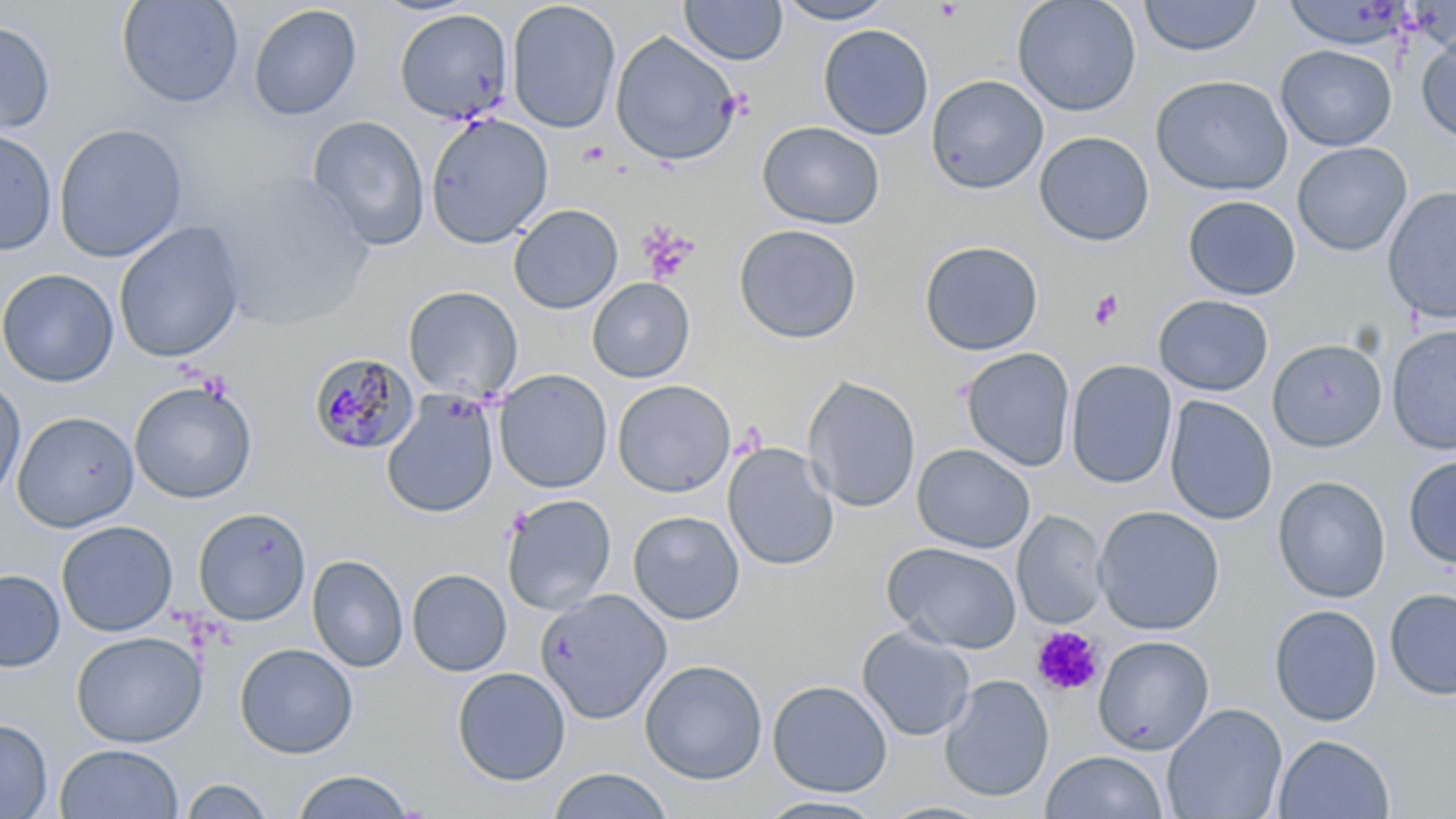
Summary:
  - Coordinate format: approximate bounding boxes as named x1/y1/x2/y2 corners in pixels
  - Platelet locations: (x1=637, y1=222, x2=699, y2=285), (x1=1088, y1=289, x2=1124, y2=330), (x1=1032, y1=626, x2=1105, y2=697)
  - Plasmodium malariae-infected red blood cell locations: (x1=308, y1=352, x2=419, y2=455)
  - Uninfected red blood cell locations: (x1=117, y1=0, x2=244, y2=108), (x1=679, y1=0, x2=788, y2=65), (x1=774, y1=0, x2=897, y2=25), (x1=1012, y1=0, x2=1142, y2=117), (x1=1138, y1=0, x2=1263, y2=57), (x1=506, y1=1, x2=621, y2=134), (x1=248, y1=4, x2=362, y2=121), (x1=394, y1=9, x2=514, y2=125), (x1=0, y1=20, x2=56, y2=135), (x1=818, y1=24, x2=934, y2=140), (x1=610, y1=30, x2=742, y2=166), (x1=1416, y1=32, x2=1456, y2=145), (x1=1275, y1=44, x2=1397, y2=151), (x1=926, y1=74, x2=1049, y2=194), (x1=1150, y1=74, x2=1293, y2=196), (x1=425, y1=113, x2=553, y2=249), (x1=307, y1=115, x2=430, y2=250), (x1=757, y1=121, x2=885, y2=229), (x1=53, y1=123, x2=189, y2=263), (x1=0, y1=128, x2=57, y2=255), (x1=1034, y1=131, x2=1154, y2=246), (x1=1292, y1=141, x2=1412, y2=256), (x1=206, y1=173, x2=378, y2=332), (x1=1382, y1=186, x2=1456, y2=325), (x1=1183, y1=195, x2=1301, y2=300), (x1=509, y1=204, x2=623, y2=314), (x1=112, y1=221, x2=247, y2=364), (x1=733, y1=223, x2=862, y2=344), (x1=919, y1=240, x2=1044, y2=356), (x1=0, y1=268, x2=119, y2=387), (x1=587, y1=277, x2=695, y2=383), (x1=403, y1=286, x2=523, y2=401), (x1=1153, y1=294, x2=1274, y2=396), (x1=1386, y1=323, x2=1456, y2=455), (x1=1267, y1=338, x2=1388, y2=452), (x1=961, y1=347, x2=1076, y2=471), (x1=1066, y1=360, x2=1177, y2=489), (x1=494, y1=369, x2=612, y2=493), (x1=0, y1=375, x2=26, y2=503), (x1=802, y1=375, x2=921, y2=513), (x1=129, y1=379, x2=257, y2=503), (x1=612, y1=379, x2=737, y2=498), (x1=381, y1=390, x2=500, y2=518), (x1=1164, y1=395, x2=1278, y2=525), (x1=12, y1=411, x2=140, y2=533), (x1=722, y1=442, x2=839, y2=571), (x1=912, y1=443, x2=1035, y2=554), (x1=1403, y1=455, x2=1456, y2=569), (x1=1273, y1=475, x2=1391, y2=603), (x1=501, y1=494, x2=617, y2=615), (x1=1092, y1=505, x2=1225, y2=635), (x1=193, y1=507, x2=311, y2=626), (x1=628, y1=510, x2=745, y2=625), (x1=1013, y1=510, x2=1108, y2=629), (x1=56, y1=520, x2=178, y2=637), (x1=882, y1=541, x2=1022, y2=653), (x1=307, y1=554, x2=409, y2=672), (x1=406, y1=568, x2=512, y2=676), (x1=0, y1=569, x2=65, y2=672), (x1=1385, y1=588, x2=1456, y2=700), (x1=536, y1=589, x2=672, y2=724), (x1=1269, y1=604, x2=1383, y2=726), (x1=857, y1=626, x2=975, y2=741), (x1=71, y1=631, x2=206, y2=747), (x1=1092, y1=635, x2=1214, y2=755), (x1=234, y1=643, x2=358, y2=759), (x1=639, y1=659, x2=768, y2=784), (x1=452, y1=666, x2=571, y2=786), (x1=940, y1=674, x2=1054, y2=802), (x1=767, y1=679, x2=892, y2=797), (x1=1161, y1=703, x2=1288, y2=819), (x1=0, y1=718, x2=53, y2=818), (x1=1273, y1=733, x2=1396, y2=819), (x1=54, y1=743, x2=184, y2=819), (x1=1041, y1=751, x2=1168, y2=819), (x1=548, y1=768, x2=673, y2=819), (x1=290, y1=769, x2=416, y2=818), (x1=177, y1=776, x2=277, y2=818), (x1=755, y1=795, x2=888, y2=818)
  - Slide-level diagnosis: Plasmodium malariae
  - Modality: optical microscopy
  - Image size: 1456×819 pixels
  - Preparation: thin blood smear
  - Stain: May-Grünwald-Giemsa
  - Field of view: one of a larger specimen
  - Magnification: 1000x